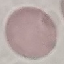

malaria status = uninfected
stain = Giemsa
image type = automatically extracted cell patch, resized to 64 × 64 pixels
preparation = thin smear
capture = smartphone through the microscope eyepiece